Locate every Plasmodium ovale-infected red blood cell.
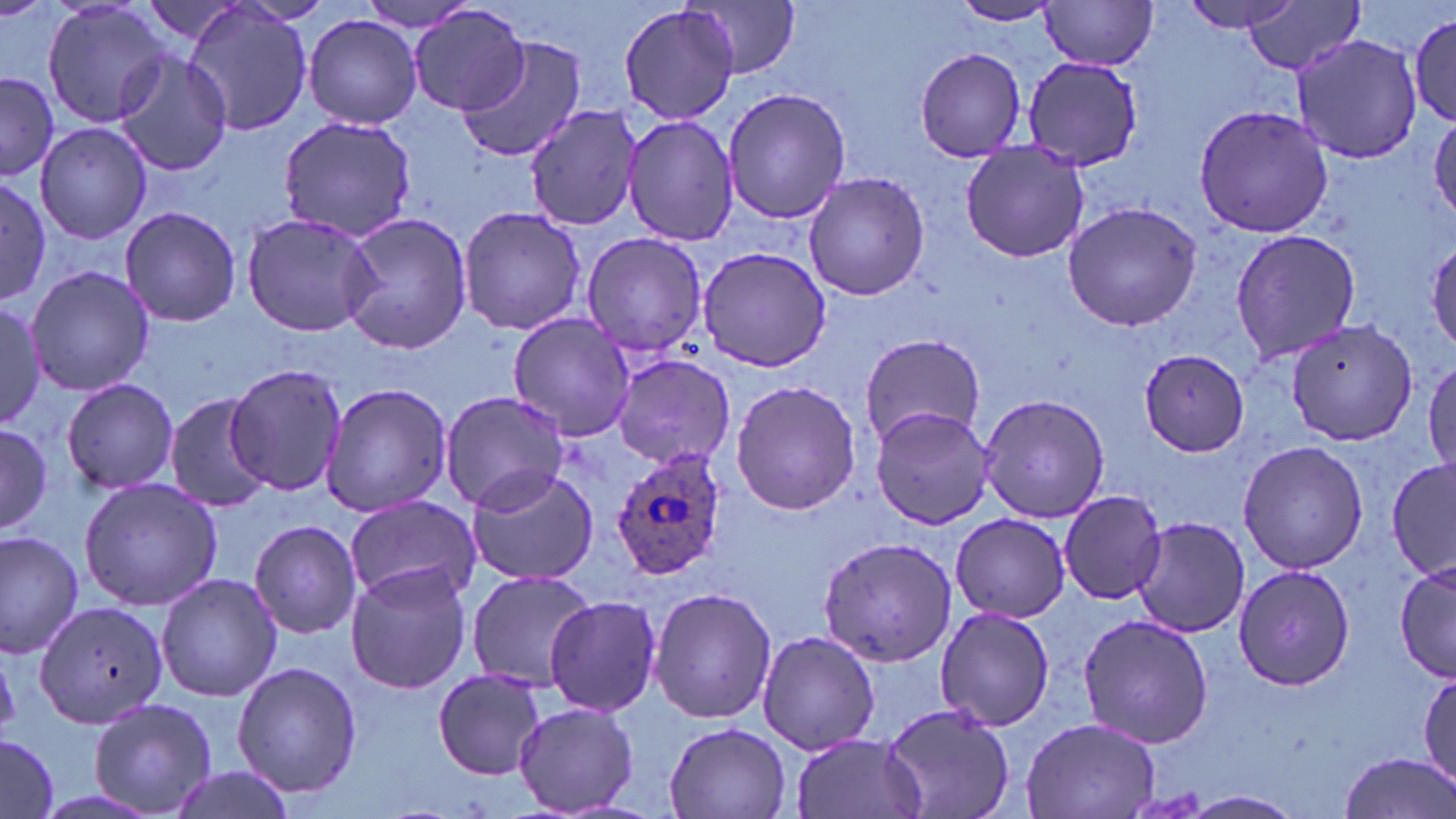
Approximate bounding boxes as [x1, y1, x2, y2] in pixels.
Plasmodium ovale-infected red blood cells: [608, 442, 731, 581].

Summary:
  - Uninfected red blood cell locations: [349, 0, 487, 33], [1176, 0, 1304, 33], [42, 1, 174, 126], [679, 1, 804, 78], [1039, 1, 1161, 70], [948, 2, 1062, 26], [1239, 2, 1361, 77], [182, 4, 314, 138], [409, 4, 528, 116], [617, 5, 740, 126], [1409, 10, 1456, 128], [304, 14, 422, 129], [1291, 33, 1425, 164], [455, 34, 588, 163], [913, 47, 1026, 162], [110, 49, 234, 179], [1022, 55, 1142, 171], [0, 72, 58, 182], [723, 86, 850, 225], [1193, 102, 1332, 239], [524, 103, 644, 233], [620, 111, 739, 247], [278, 113, 416, 242], [1429, 114, 1456, 223], [33, 121, 155, 245], [959, 139, 1092, 265], [802, 172, 929, 301], [0, 176, 53, 303], [1062, 201, 1204, 332], [458, 205, 587, 336], [118, 207, 243, 327], [239, 211, 384, 339], [337, 212, 475, 355], [1227, 228, 1363, 364], [579, 231, 707, 357], [697, 246, 836, 372], [26, 265, 155, 396], [0, 299, 51, 426], [506, 312, 635, 442], [1284, 319, 1421, 444], [859, 333, 987, 450], [1141, 348, 1252, 456], [611, 355, 735, 469], [1425, 357, 1456, 484], [225, 364, 347, 496], [63, 376, 180, 496], [730, 379, 860, 517], [321, 382, 452, 518], [438, 388, 571, 516], [980, 391, 1109, 524], [163, 393, 274, 511], [869, 405, 998, 532], [0, 422, 52, 537], [1237, 440, 1368, 575], [1387, 458, 1456, 582], [464, 463, 599, 587], [79, 477, 225, 610], [1057, 489, 1169, 605], [342, 498, 479, 601], [953, 512, 1072, 620], [1131, 515, 1250, 638], [248, 519, 363, 641], [0, 528, 81, 655], [816, 535, 958, 666], [1393, 557, 1454, 682], [345, 562, 475, 695], [1234, 565, 1356, 692], [463, 569, 595, 690], [154, 572, 281, 701], [648, 586, 777, 725], [543, 595, 663, 716], [33, 599, 166, 727], [936, 606, 1057, 730], [1078, 612, 1213, 749], [757, 630, 881, 755], [231, 662, 364, 798], [1419, 668, 1456, 786], [432, 669, 547, 779], [88, 697, 217, 817], [512, 700, 638, 817], [877, 701, 1021, 819], [1020, 716, 1163, 818], [664, 722, 792, 818], [789, 732, 927, 819], [0, 736, 58, 819], [1336, 753, 1454, 819], [164, 766, 298, 819], [1180, 790, 1306, 819]
  - Slide-level diagnosis: Plasmodium ovale
  - Preparation: thin blood smear
  - Field of view: single
  - Image size: 1456×819 pixels
  - Magnification: 1000x
  - Modality: optical microscopy
  - Stain: May-Grünwald-Giemsa